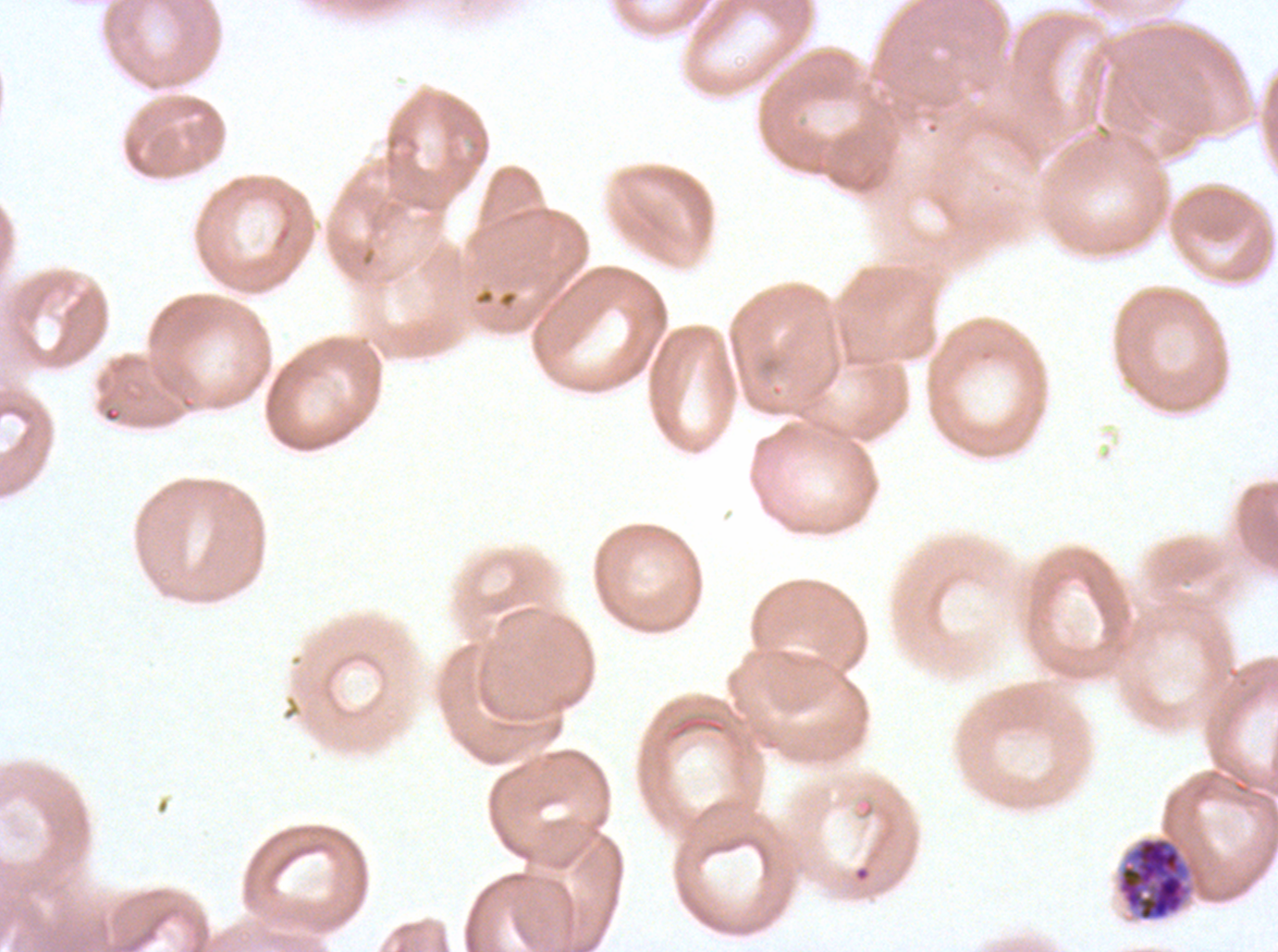
Approximate bounding boxes as (x1, y1, x2, y2) in pixels.
Summary:
  - Early schizont locations: (1117, 836, 1191, 921)
  - Stain: Giemsa
  - Preparation: thin blood smear
  - Specimen: P. falciparum from a patient in The Gambia, cultured ex vivo for 24 to 48 hours
  - Image size: 1278×952 pixels
  - Field of view: one sub-image of a larger composite